Give the extent of all Plasmodium falciparum-infected red blood cells.
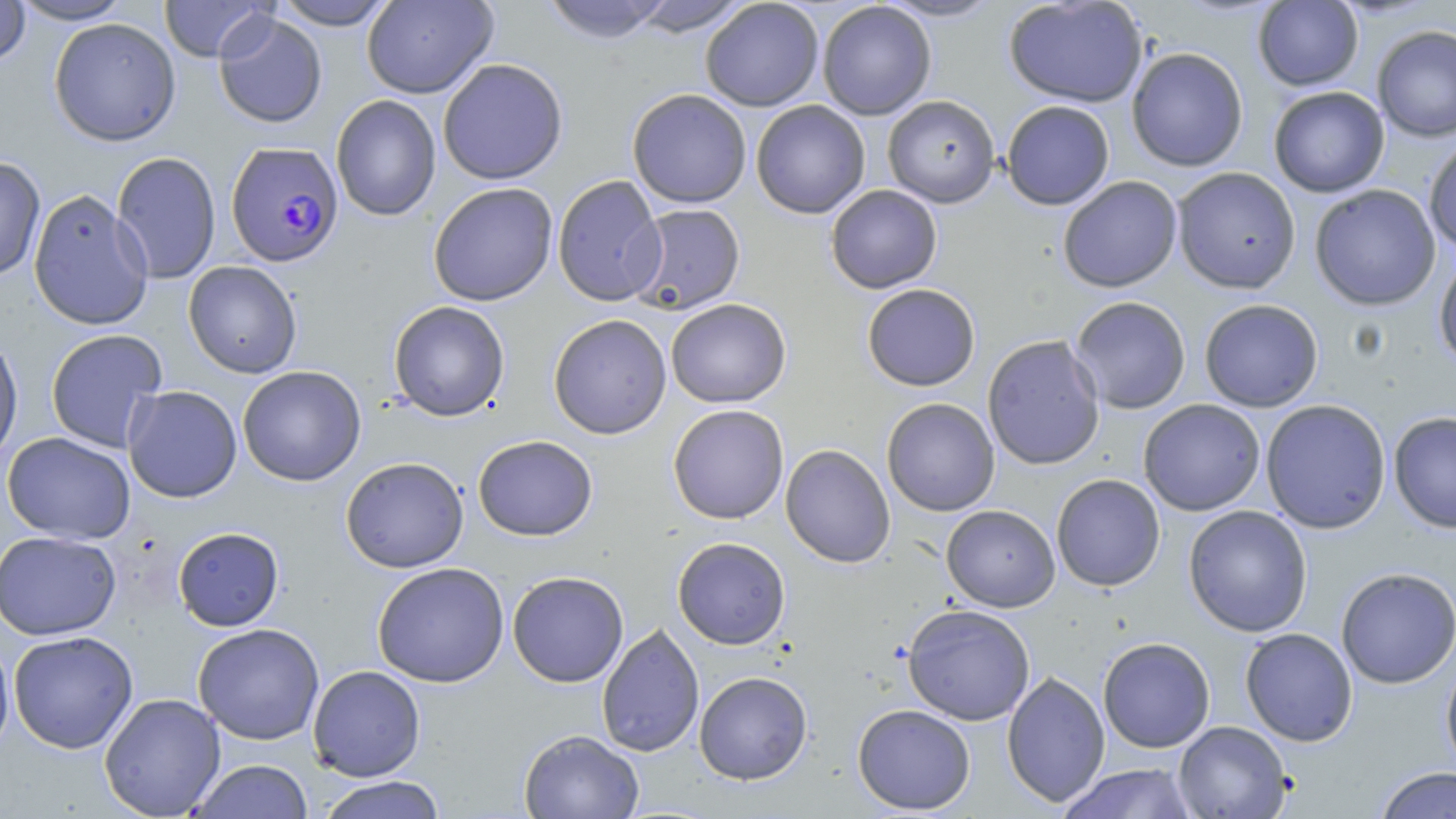
Approximate bounding boxes as named x1/y1/x2/y2 corners in pixels.
Plasmodium falciparum-infected red blood cells: (x1=225, y1=140, x2=344, y2=268).

slide-level diagnosis = Plasmodium falciparum
uninfected red blood cell locations = approximate bounding boxes as named x1/y1/x2/y2 corners in pixels: (x1=0, y1=0, x2=31, y2=67), (x1=11, y1=0, x2=132, y2=24), (x1=159, y1=0, x2=273, y2=62), (x1=272, y1=0, x2=396, y2=30), (x1=362, y1=0, x2=498, y2=99), (x1=540, y1=0, x2=674, y2=44), (x1=876, y1=0, x2=1005, y2=22), (x1=1002, y1=0, x2=1148, y2=108), (x1=628, y1=1, x2=751, y2=36), (x1=700, y1=1, x2=824, y2=112), (x1=817, y1=1, x2=936, y2=120), (x1=1253, y1=1, x2=1363, y2=91), (x1=213, y1=11, x2=328, y2=128), (x1=48, y1=17, x2=181, y2=146), (x1=1371, y1=26, x2=1456, y2=143), (x1=1126, y1=47, x2=1249, y2=172), (x1=438, y1=58, x2=568, y2=185), (x1=1268, y1=86, x2=1389, y2=197), (x1=627, y1=89, x2=752, y2=208), (x1=330, y1=94, x2=441, y2=221), (x1=882, y1=95, x2=1000, y2=208), (x1=751, y1=100, x2=870, y2=218), (x1=1001, y1=100, x2=1115, y2=210), (x1=1424, y1=137, x2=1456, y2=254), (x1=111, y1=151, x2=221, y2=284), (x1=0, y1=155, x2=46, y2=282), (x1=1172, y1=167, x2=1301, y2=294), (x1=552, y1=175, x2=667, y2=307), (x1=1058, y1=176, x2=1182, y2=293), (x1=428, y1=182, x2=558, y2=306), (x1=1309, y1=184, x2=1441, y2=311), (x1=825, y1=185, x2=942, y2=293), (x1=28, y1=189, x2=153, y2=331), (x1=628, y1=203, x2=746, y2=315), (x1=1434, y1=253, x2=1456, y2=370), (x1=183, y1=261, x2=302, y2=378), (x1=862, y1=284, x2=980, y2=391), (x1=1070, y1=296, x2=1191, y2=414), (x1=665, y1=298, x2=791, y2=408), (x1=1199, y1=299, x2=1323, y2=412), (x1=388, y1=301, x2=510, y2=421), (x1=548, y1=314, x2=672, y2=439), (x1=45, y1=329, x2=168, y2=452), (x1=0, y1=330, x2=23, y2=468), (x1=981, y1=334, x2=1105, y2=470), (x1=237, y1=366, x2=366, y2=486), (x1=122, y1=385, x2=243, y2=503), (x1=881, y1=398, x2=1000, y2=516), (x1=1138, y1=399, x2=1265, y2=516), (x1=1260, y1=399, x2=1391, y2=534), (x1=668, y1=405, x2=789, y2=524), (x1=1388, y1=411, x2=1456, y2=533), (x1=2, y1=432, x2=136, y2=544), (x1=472, y1=435, x2=598, y2=541), (x1=780, y1=444, x2=896, y2=568), (x1=341, y1=456, x2=469, y2=573), (x1=1051, y1=474, x2=1165, y2=591), (x1=941, y1=504, x2=1060, y2=611), (x1=1183, y1=505, x2=1313, y2=637), (x1=173, y1=526, x2=284, y2=631), (x1=0, y1=531, x2=121, y2=640), (x1=672, y1=537, x2=790, y2=649), (x1=372, y1=562, x2=510, y2=687), (x1=1335, y1=567, x2=1456, y2=689), (x1=507, y1=571, x2=629, y2=687), (x1=902, y1=604, x2=1036, y2=725), (x1=192, y1=623, x2=325, y2=745), (x1=596, y1=623, x2=705, y2=757), (x1=1240, y1=628, x2=1357, y2=746), (x1=7, y1=630, x2=138, y2=754), (x1=0, y1=631, x2=16, y2=761), (x1=1098, y1=637, x2=1215, y2=752), (x1=1441, y1=654, x2=1456, y2=778), (x1=307, y1=665, x2=426, y2=781), (x1=694, y1=671, x2=812, y2=784), (x1=1002, y1=671, x2=1110, y2=808), (x1=99, y1=693, x2=226, y2=818), (x1=852, y1=704, x2=976, y2=815), (x1=1173, y1=721, x2=1291, y2=818), (x1=518, y1=729, x2=645, y2=819), (x1=189, y1=759, x2=313, y2=819), (x1=1058, y1=763, x2=1198, y2=819), (x1=1374, y1=766, x2=1456, y2=818), (x1=316, y1=776, x2=448, y2=819)
image size = 1456×819 pixels
modality = optical microscopy
field of view = one of a larger specimen
magnification = 1000x
stain = May-Grünwald-Giemsa
preparation = thin blood smear